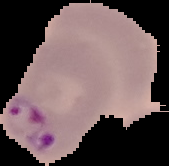

From a thin blood smear. Image is 169×166 pixels. Cell region segmented out of the field of view; the surrounding area is masked to black. Result: Plasmodium parasites identified.